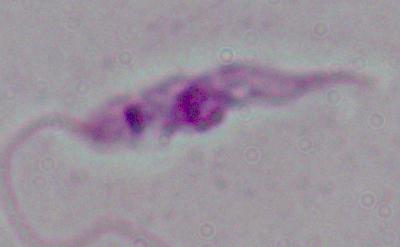

{
  "identification": "Leishmania",
  "magnification": "1000x",
  "modality": "photomicrograph"
}